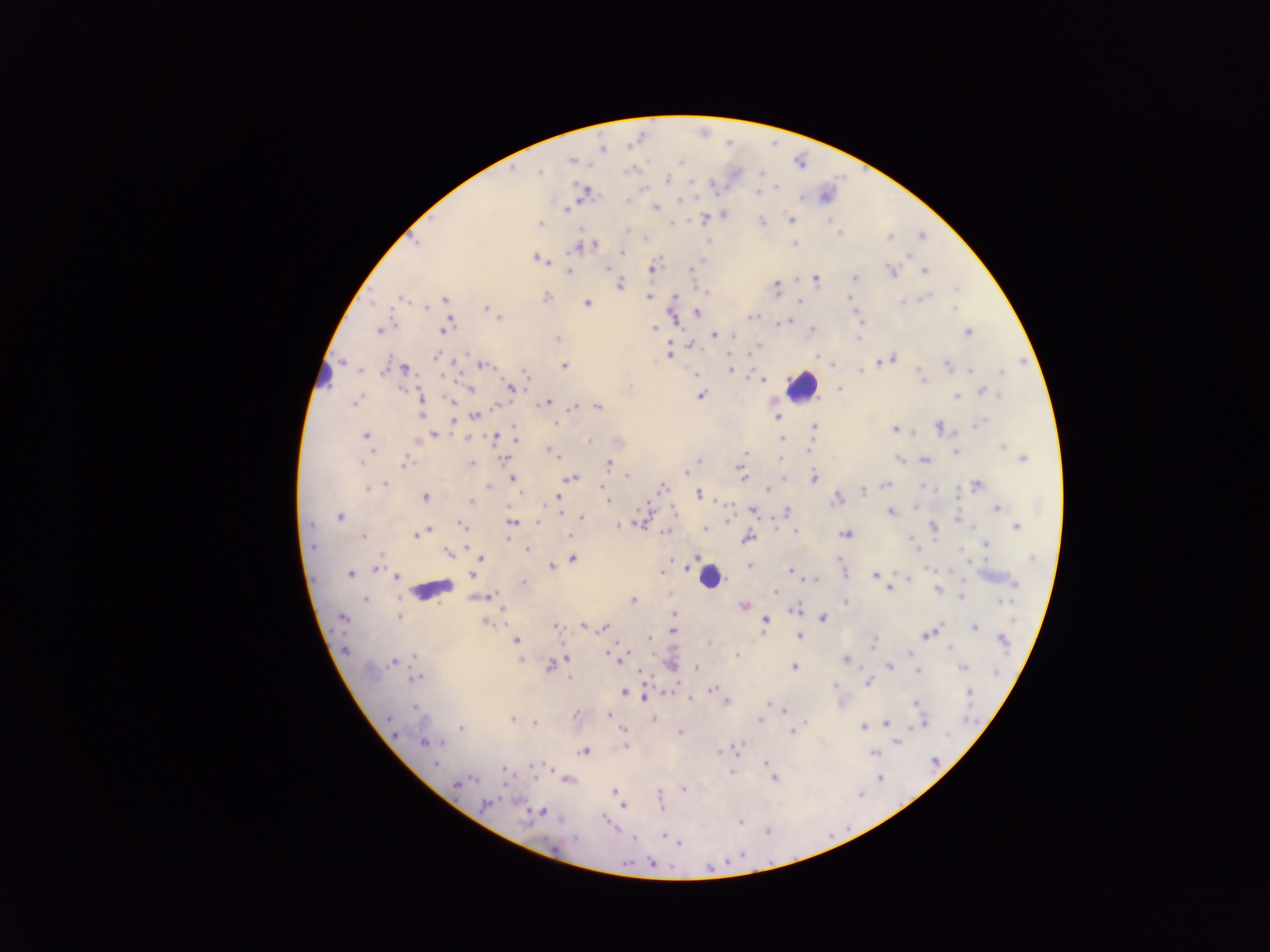
Approximate centers as {x, y} in pixels.
Summary:
  - Malaria parasite locations: {602, 149}, {572, 161}, {679, 161}, {539, 171}, {667, 180}, {776, 187}, {757, 192}, {584, 193}, {628, 200}, {680, 200}, {656, 207}, {566, 209}, {724, 215}, {704, 219}, {790, 219}, {829, 220}, {540, 223}, {762, 223}, {627, 230}, {839, 233}, {923, 235}, {890, 237}, {415, 242}, {795, 244}, {588, 246}, {579, 247}, {622, 252}, {910, 256}, {705, 258}, {536, 259}, {702, 261}, {606, 269}, {652, 269}, {692, 270}, {925, 270}, {569, 271}, {892, 271}, {855, 277}, {816, 279}, {620, 285}, {776, 288}, {957, 289}, {648, 297}, {402, 298}, {546, 298}, {927, 298}, {445, 300}, {800, 301}, {901, 302}, {372, 303}, {588, 304}, {426, 307}, {487, 309}, {954, 309}, {697, 312}, {856, 314}, {752, 316}, {498, 318}, {780, 322}, {786, 322}, {793, 322}, {393, 324}, {654, 328}, {446, 329}, {812, 329}, {379, 331}, {968, 332}, {714, 335}, {733, 336}, {859, 338}, {557, 339}, {692, 344}, {759, 346}, {669, 354}, {436, 356}, {817, 357}, {892, 358}, {882, 361}, {482, 365}, {564, 366}, {948, 366}, {403, 369}, {730, 369}, {361, 370}, {860, 371}, {971, 371}, {1002, 373}, {524, 374}, {762, 380}, {922, 380}, {630, 388}, {840, 388}, {469, 389}, {512, 389}, {984, 392}, {993, 394}, {701, 396}, {957, 396}, {421, 398}, {452, 401}, {354, 403}, {546, 403}, {496, 406}, {573, 407}, {597, 407}, {422, 413}, {475, 415}, {777, 417}, {453, 421}, {980, 423}, {556, 425}, {814, 427}, {940, 427}, {514, 429}, {895, 429}, {434, 434}, {366, 436}, {495, 438}, {781, 438}, {417, 440}, {589, 442}, {1003, 446}, {549, 451}, {808, 451}, {955, 452}, {745, 453}, {553, 454}, {1023, 458}, {504, 459}, {780, 460}, {899, 460}, {925, 460}, {698, 461}, {361, 462}, {609, 462}, {405, 463}, {471, 464}, {686, 472}, {742, 474}, {627, 475}, {571, 478}, {813, 478}, {512, 479}, {385, 483}, {977, 484}, {886, 485}, {487, 487}, {602, 487}, {924, 487}, {368, 488}, {662, 488}, {768, 490}, {862, 492}, {699, 494}, {958, 496}, {425, 497}, {557, 498}, {607, 499}, {837, 499}, {470, 502}, {996, 508}, {753, 510}, {560, 511}, {787, 511}, {891, 513}, {339, 516}, {582, 518}, {958, 519}, {640, 521}, {511, 522}, {538, 522}, {776, 523}, {311, 525}, {462, 526}, {933, 527}, {1017, 527}, {706, 529}, {428, 530}, {796, 531}, {666, 532}, {845, 534}, {416, 535}, {569, 536}, {363, 538}, {748, 538}, {913, 541}, {312, 545}, {986, 545}, {916, 548}, {527, 550}, {962, 550}, {449, 554}, {382, 555}, {480, 558}, {1032, 558}, {573, 559}, {551, 566}, {749, 566}, {376, 569}, {790, 571}, {662, 572}, {844, 572}, {350, 574}, {471, 575}, {875, 575}, {396, 577}, {812, 579}, {908, 579}, {523, 583}, {1015, 584}, {889, 590}, {938, 590}, {776, 592}, {488, 596}, {961, 597}, {365, 601}, {633, 601}, {1003, 601}, {846, 603}, {744, 606}, {796, 609}, {673, 613}, {400, 617}, {823, 617}, {342, 618}, {765, 621}, {486, 622}, {582, 626}, {556, 627}, {603, 628}, {975, 628}, {672, 631}, {929, 633}, {800, 637}, {649, 638}, {515, 641}, {1004, 642}, {874, 643}, {950, 647}, {345, 651}, {909, 652}, {414, 655}, {613, 655}, {736, 656}, {567, 659}, {618, 659}, {846, 659}, {519, 661}, {391, 663}, {671, 665}, {550, 666}, {794, 667}, {890, 667}, {697, 668}, {963, 668}, {918, 671}, {997, 672}, {415, 678}, {570, 678}, {868, 683}, {835, 686}, {712, 689}, {971, 692}, {624, 693}, {646, 698}, {690, 699}, {728, 702}, {916, 703}, {415, 707}, {785, 712}, {575, 715}, {609, 715}, {388, 719}, {512, 719}, {654, 719}, {760, 719}, {533, 723}, {887, 723}, {923, 723}, {461, 728}, {863, 728}, {623, 730}, {793, 731}, {681, 733}, {395, 734}, {424, 743}, {441, 743}, {897, 743}, {625, 746}, {738, 748}, {583, 752}, {719, 752}, {873, 753}, {766, 763}, {434, 764}, {534, 766}, {503, 771}, {732, 772}, {774, 779}, {880, 779}, {570, 780}, {469, 781}, {458, 784}, {684, 790}, {615, 792}, {661, 798}, {485, 803}, {515, 803}, {660, 804}, {623, 806}, {541, 812}, {740, 823}, {767, 832}, {665, 836}, {576, 839}, {633, 839}, {679, 843}, {652, 863}
  - Leukocyte locations: {322, 373}, {803, 385}, {709, 576}, {432, 589}
  - Field of view: single
  - Capture: mobile-phone photograph through a microscope
  - Preparation: thick blood smear
  - Image size: 1270×952 pixels
  - Country: Ghana